Classify this cell by malaria status.
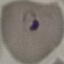

It is parasitized.

preparation = thin smear
image type = cell patch, automatically extracted from a larger field of view and resized to 64 × 64 pixels
stain = Giemsa
capture = smartphone through the microscope eyepiece